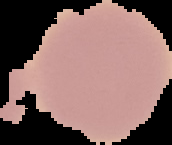

Summary:
  - Result: no malaria parasites seen
  - Image type: cell region segmented out of the field of view; surrounding area masked to black
  - Image size: 172×145 pixels
  - Preparation: thin blood smear